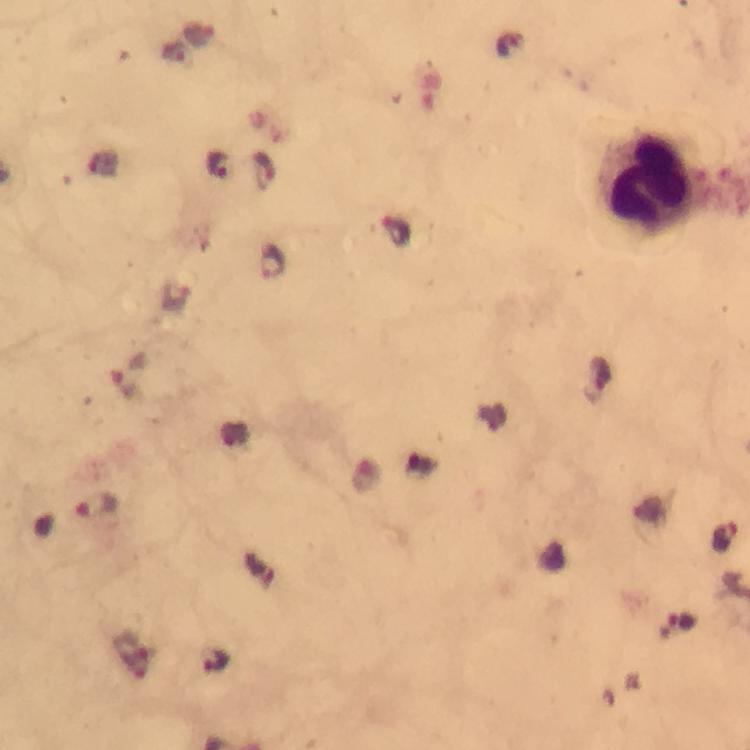
Approximate object centers, in pixels from the top-left corner.
Summary:
  - Leukocyte locations: (x=649, y=182)
  - Plasmodium parasite locations: (x=200, y=35), (x=174, y=53), (x=218, y=166), (x=264, y=170), (x=396, y=231), (x=272, y=263), (x=129, y=376), (x=97, y=505), (x=726, y=538), (x=681, y=625)
  - Image size: 750×750 pixels
  - Preparation: thick smear
  - Immersion oil: applied
  - Magnification: 100x
  - Context: from a diagnostic examination for malaria
  - Stain: Giemsa
  - Cropped from: one field of view
  - Capture: smartphone mounted on the microscope